Report the malaria status of this cell.
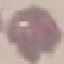
It is uninfected.

Summary:
  - Image type: cell patch, automatically extracted from a larger field of view and resized to 64 × 64 pixels
  - Preparation: thin smear
  - Capture: smartphone camera at the microscope eyepiece
  - Stain: Giemsa